Assess the morphology of the red blood cells.
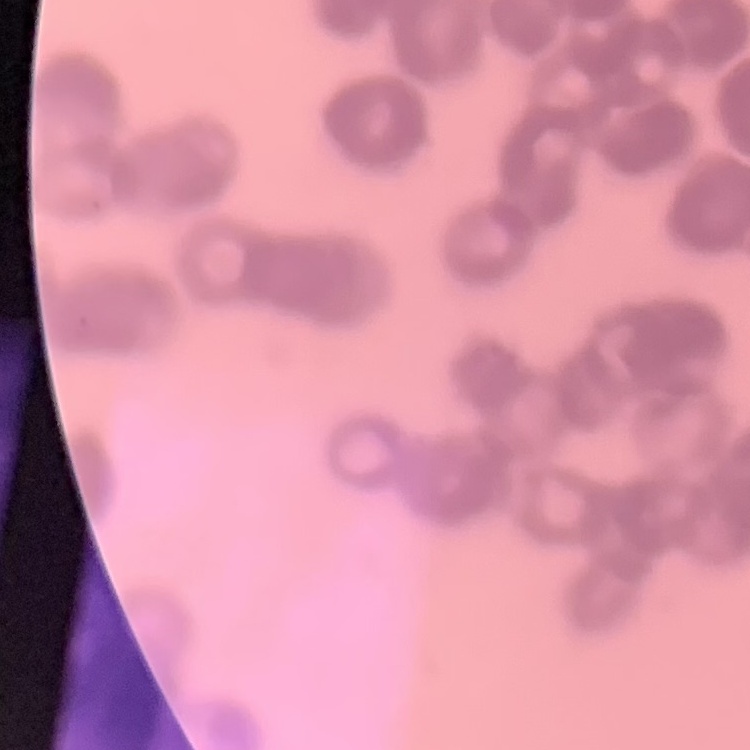

Rouleaux formation.

Summary:
  - Image type: one tile cut from a larger photomicrograph
  - Stain: Field's or Giemsa
  - Preparation: thin blood film